State the blood parasite species.
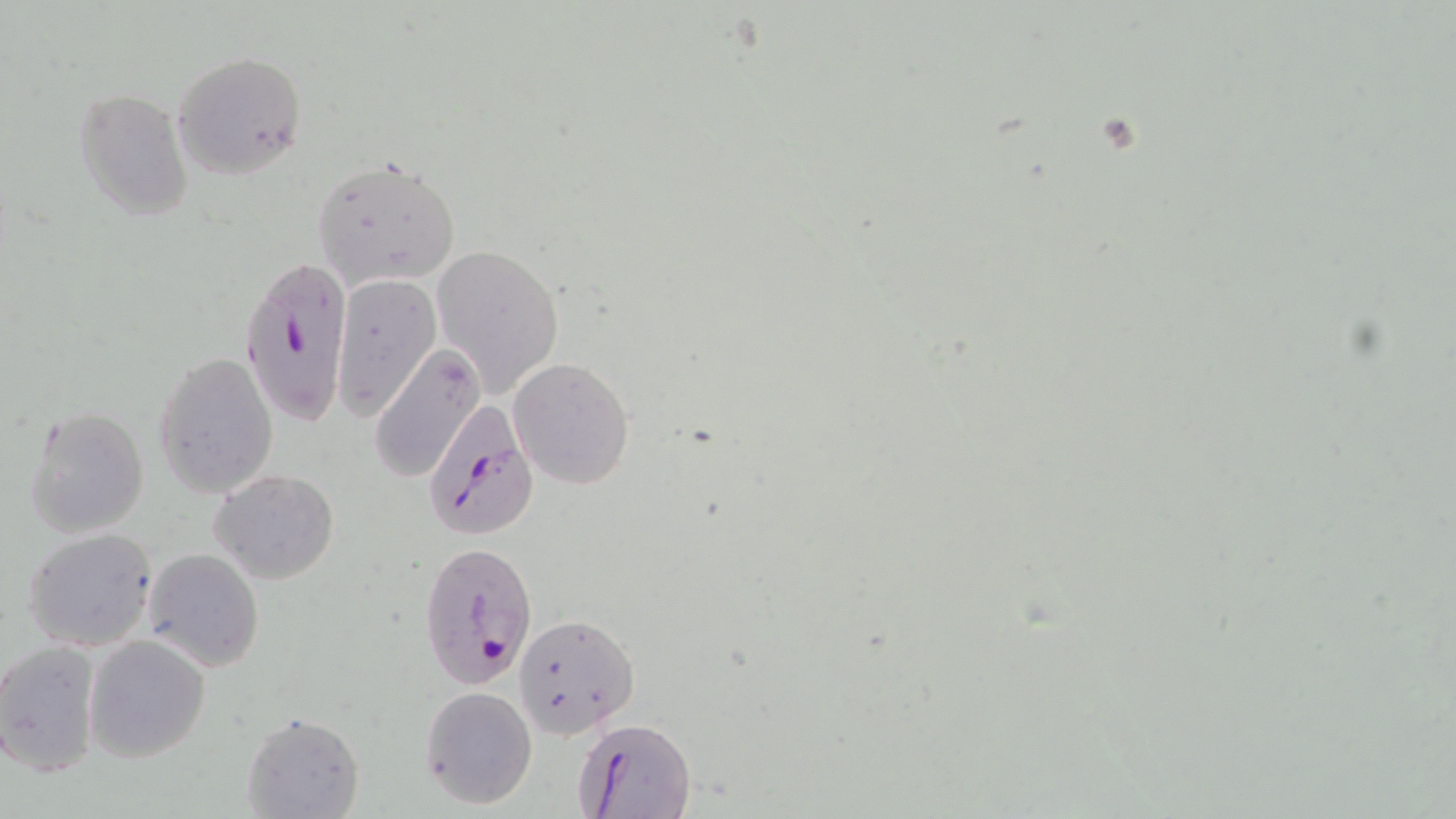

Plasmodium falciparum.

Summary:
  - Coordinate format: approximate bounding boxes as [x1, y1, x2, y2] in pixels
  - Uninfected red blood cell locations: [172, 51, 308, 179], [75, 87, 193, 222], [313, 155, 461, 290], [431, 244, 564, 400], [332, 274, 440, 418], [371, 345, 487, 483], [153, 352, 280, 498], [508, 358, 634, 489], [25, 404, 148, 540], [210, 468, 339, 586], [23, 527, 158, 651], [143, 548, 263, 672], [514, 614, 638, 737], [84, 635, 211, 761], [0, 641, 102, 777], [418, 685, 538, 810], [241, 710, 364, 819]
  - Plasmodium falciparum-infected red blood cell locations: [243, 256, 347, 436], [422, 394, 537, 535], [416, 540, 540, 692], [578, 717, 694, 819]
  - Field of view: one of a larger specimen
  - Magnification: 1000x
  - Image size: 1456×819 pixels
  - Preparation: thin blood smear
  - Modality: light microscopy
  - Stain: May-Grünwald-Giemsa